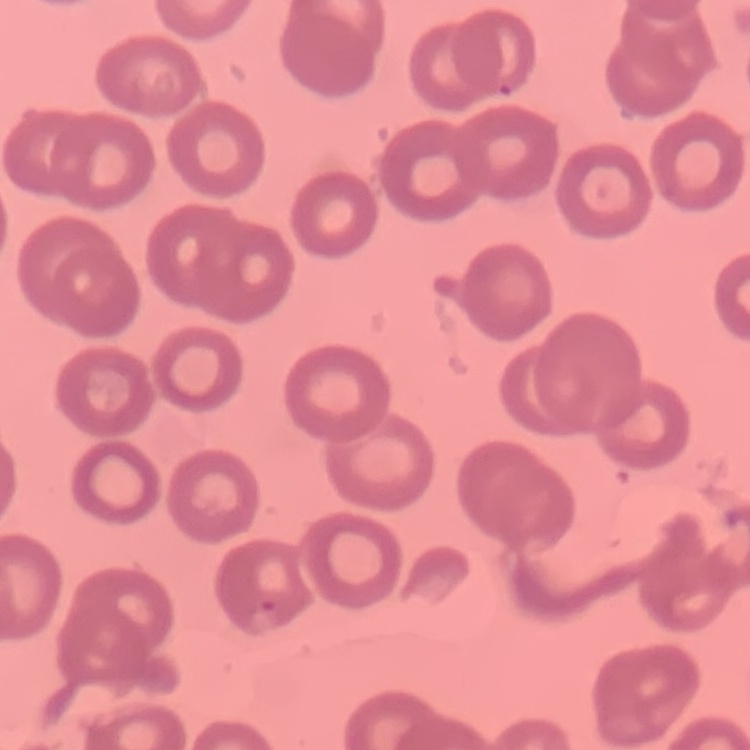 The red blood cells exhibit no rouleaux formation. Stained with either Field's or Giemsa. Thin blood smear. One tile cut from a larger photomicrograph.